State which cell type is depicted.
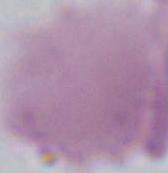
This is an erythrocyte.

modality = micrograph
magnification = 1000x